Locate every Plasmodium parasite.
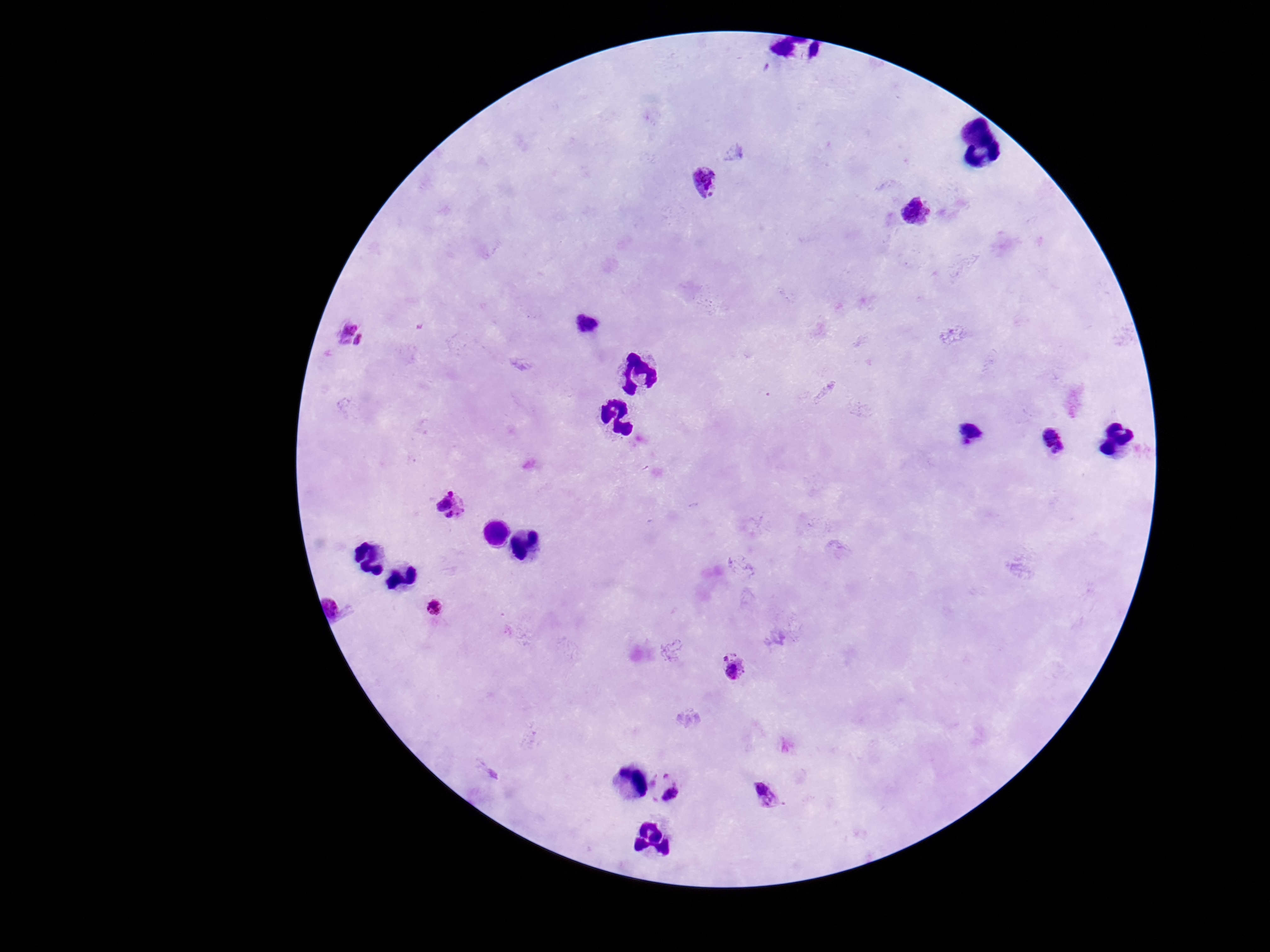
Approximate centers as (x, y) in pixels.
Plasmodium parasites: (701, 178), (918, 213), (586, 323), (352, 334), (971, 434), (1055, 442), (452, 505), (437, 608), (732, 667), (667, 787), (764, 794).

field of view = one from this slide
stain = Giemsa
preparation = thick blood smear
capture = smartphone camera through the microscope eyepiece
magnification = 100x
patient malaria status = infected
image size = 1270×952 pixels